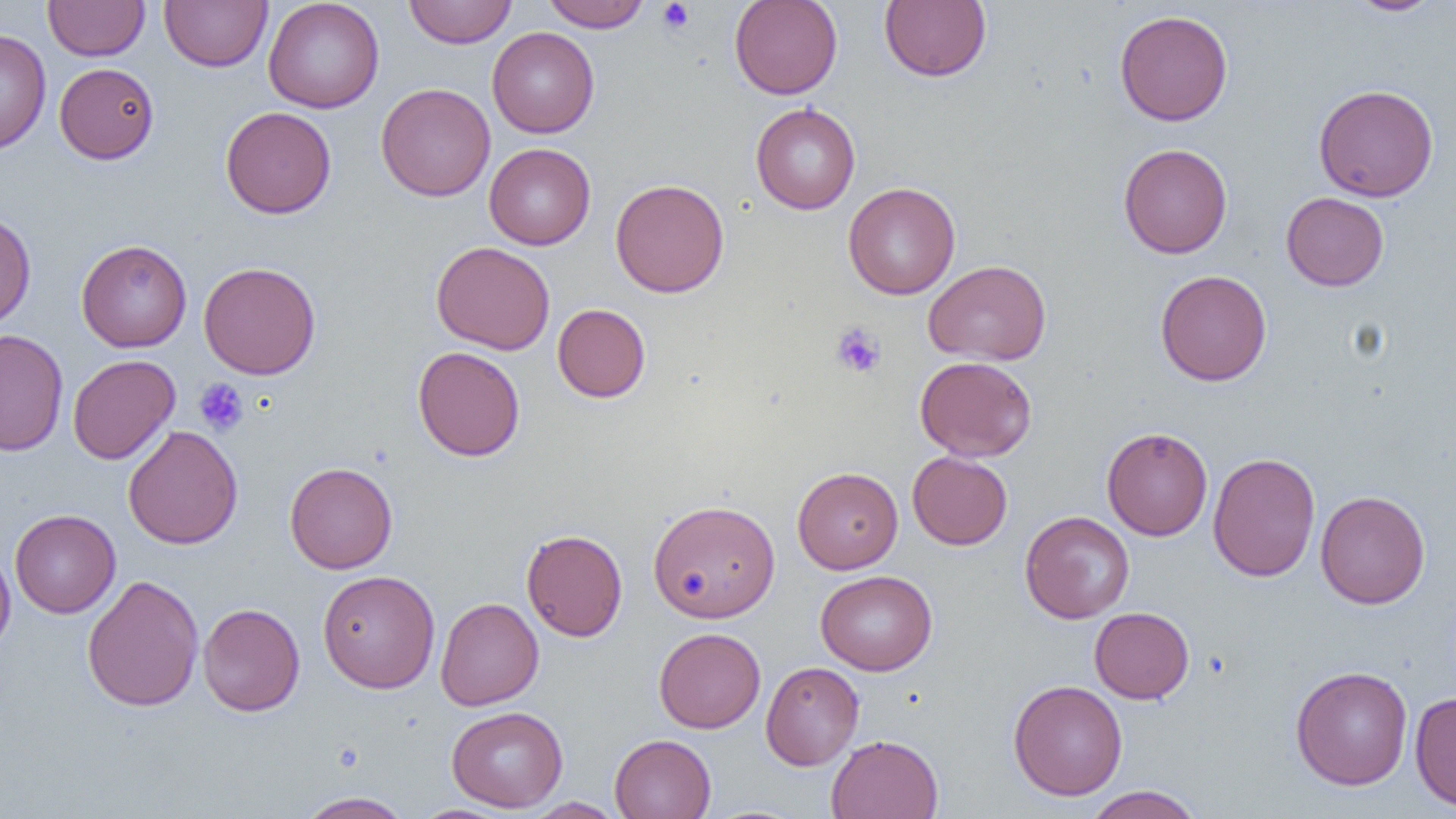

Summary:
  - Coordinate format: approximate bounding boxes as named x1/y1/x2/y2 corners in pixels
  - Uninfected red blood cell locations: (x1=43, y1=0, x2=149, y2=61), (x1=160, y1=0, x2=272, y2=71), (x1=262, y1=0, x2=384, y2=113), (x1=403, y1=0, x2=517, y2=48), (x1=729, y1=0, x2=843, y2=99), (x1=879, y1=0, x2=991, y2=82), (x1=1345, y1=0, x2=1446, y2=16), (x1=541, y1=1, x2=652, y2=32), (x1=1114, y1=9, x2=1233, y2=126), (x1=487, y1=27, x2=599, y2=138), (x1=0, y1=28, x2=51, y2=155), (x1=54, y1=63, x2=159, y2=164), (x1=375, y1=82, x2=495, y2=202), (x1=1313, y1=84, x2=1439, y2=202), (x1=750, y1=102, x2=860, y2=214), (x1=220, y1=106, x2=336, y2=218), (x1=484, y1=143, x2=596, y2=250), (x1=1118, y1=143, x2=1233, y2=259), (x1=610, y1=179, x2=729, y2=297), (x1=843, y1=181, x2=961, y2=299), (x1=1281, y1=192, x2=1389, y2=291), (x1=0, y1=208, x2=36, y2=331), (x1=76, y1=239, x2=192, y2=352), (x1=431, y1=241, x2=555, y2=355), (x1=924, y1=259, x2=1052, y2=365), (x1=198, y1=261, x2=321, y2=379), (x1=1155, y1=269, x2=1272, y2=386), (x1=552, y1=303, x2=651, y2=403), (x1=1, y1=329, x2=68, y2=456), (x1=413, y1=346, x2=525, y2=461), (x1=67, y1=354, x2=180, y2=464), (x1=915, y1=356, x2=1037, y2=461), (x1=123, y1=425, x2=243, y2=549), (x1=1101, y1=426, x2=1213, y2=541), (x1=1102, y1=437, x2=1322, y2=553), (x1=907, y1=451, x2=1012, y2=550), (x1=1208, y1=452, x2=1320, y2=582), (x1=285, y1=461, x2=398, y2=574), (x1=792, y1=467, x2=903, y2=574), (x1=1315, y1=490, x2=1431, y2=609), (x1=648, y1=498, x2=780, y2=623), (x1=9, y1=509, x2=121, y2=618), (x1=1020, y1=510, x2=1134, y2=623), (x1=522, y1=528, x2=628, y2=642), (x1=0, y1=544, x2=16, y2=658), (x1=317, y1=570, x2=440, y2=692), (x1=816, y1=570, x2=937, y2=675), (x1=82, y1=574, x2=203, y2=712), (x1=435, y1=597, x2=544, y2=711), (x1=198, y1=602, x2=305, y2=717), (x1=1089, y1=607, x2=1194, y2=704), (x1=653, y1=627, x2=766, y2=733), (x1=761, y1=661, x2=864, y2=770), (x1=1290, y1=665, x2=1413, y2=790), (x1=1007, y1=679, x2=1128, y2=800), (x1=1409, y1=691, x2=1456, y2=812), (x1=446, y1=706, x2=567, y2=812), (x1=609, y1=734, x2=716, y2=819), (x1=826, y1=734, x2=943, y2=819), (x1=1083, y1=785, x2=1204, y2=819), (x1=295, y1=791, x2=414, y2=819), (x1=522, y1=797, x2=626, y2=818)
  - Platelet locations: (x1=657, y1=1, x2=695, y2=34), (x1=831, y1=324, x2=886, y2=378), (x1=194, y1=378, x2=248, y2=436)
  - Slide-level diagnosis: no evidence of blood parasites
  - Image size: 1456×819 pixels
  - Modality: optical microscopy
  - Magnification: 1000x
  - Preparation: thin blood film
  - Field of view: one of a larger specimen